Identify the preparation type.
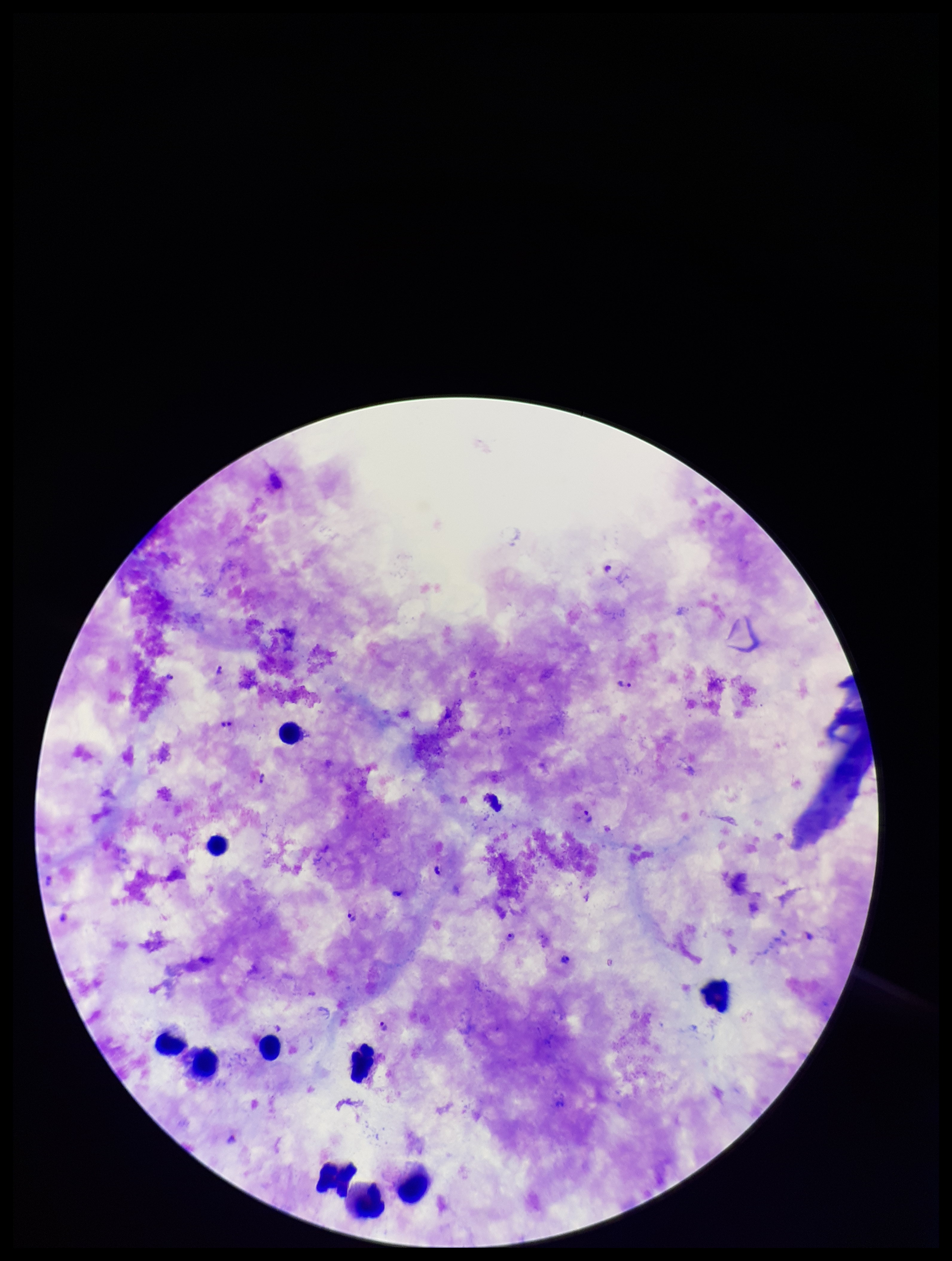

A thick smear.

Plasmodium parasites: seen. Patient malaria status: infected. Species reported for this patient: Plasmodium falciparum. Parasite count: 10. Stained with Giemsa. Image is 952×1261 pixels. Photographed through the microscope eyepiece with a smartphone camera. Leukocyte count: 10. One field from this slide.